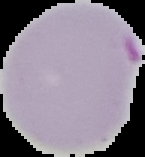

Image is 145×157 pixels. The area outside the segmented cell region is set to black. Result: Plasmodium parasites identified. From a thin blood smear.